Give the position of every Plasmodium parasite.
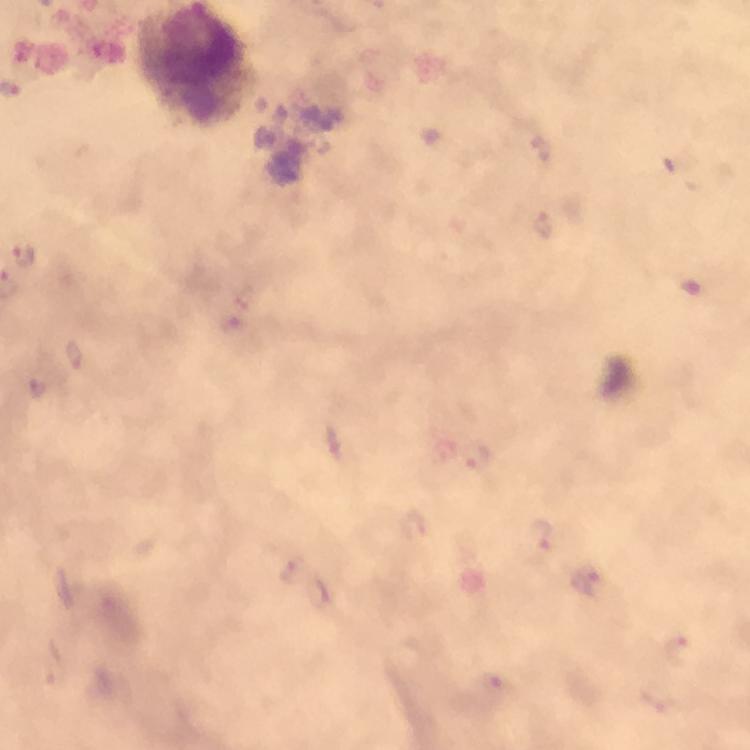
Approximate centers as [x, y] in pixels.
Plasmodium parasites: [25, 257], [75, 357], [39, 389], [477, 457], [542, 536], [293, 570], [587, 578].

magnification = 100x
stain = Giemsa
preparation = thick smear
context = from a malaria diagnostic workup
image size = 750×750 pixels
immersion oil = applied
capture = smartphone mounted on the microscope
cropped from = a single field of view
leukocyte locations = approximate centers as [x, y] in pixels: [194, 67]